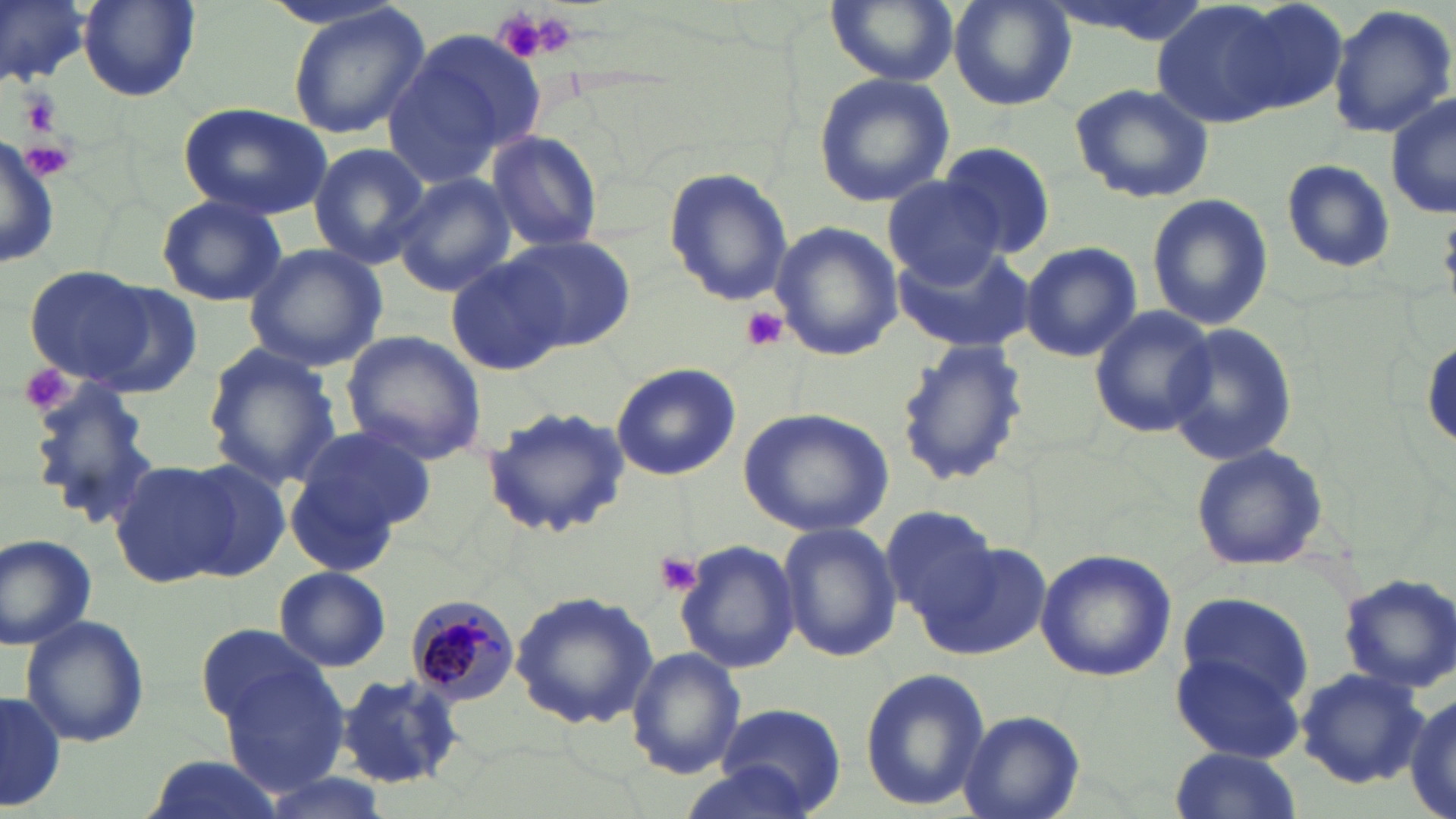

Approximate bounding boxes as (x1, y1, x2, y2) in pixels. Plasmodium malariae-infected red blood cell locations: (405, 594, 519, 707). Uninfected red blood cell locations: (0, 0, 89, 87), (824, 0, 959, 86), (948, 0, 1077, 111), (1149, 0, 1308, 130), (1210, 0, 1352, 120), (78, 1, 201, 102), (286, 3, 431, 141), (1327, 5, 1456, 140), (385, 27, 549, 185), (811, 72, 955, 209), (1068, 82, 1215, 205), (1387, 96, 1455, 221), (176, 101, 334, 220), (0, 131, 58, 276), (486, 133, 604, 255), (307, 142, 430, 269), (939, 143, 1056, 258), (1280, 159, 1396, 276), (662, 165, 793, 307), (390, 172, 517, 297), (881, 174, 1008, 287), (156, 193, 286, 308), (1145, 193, 1274, 330), (770, 223, 903, 361), (506, 235, 637, 349), (1019, 240, 1141, 363), (243, 242, 389, 371), (891, 245, 1031, 353), (444, 255, 568, 377), (23, 264, 156, 386), (80, 280, 206, 397), (1087, 305, 1216, 438), (1162, 320, 1299, 466), (341, 331, 486, 465), (1421, 334, 1455, 453), (893, 336, 1029, 490), (202, 343, 341, 489), (611, 363, 740, 481), (20, 378, 166, 531), (480, 405, 632, 543), (738, 407, 895, 537), (286, 431, 430, 571), (1189, 445, 1331, 572), (176, 461, 294, 583), (110, 462, 232, 588), (881, 505, 1000, 621), (776, 522, 901, 661), (0, 533, 96, 649), (918, 537, 1052, 661), (672, 538, 802, 674), (1034, 548, 1176, 684), (273, 565, 392, 671), (1337, 573, 1456, 693), (510, 591, 660, 729), (1169, 595, 1315, 756), (19, 612, 149, 749), (197, 624, 329, 728), (626, 646, 747, 778), (219, 662, 353, 795), (858, 667, 991, 811), (1295, 668, 1428, 789), (334, 671, 468, 789), (1, 689, 63, 814), (1405, 694, 1456, 819), (717, 699, 849, 814), (956, 710, 1084, 819), (1167, 748, 1305, 819), (137, 753, 285, 819), (676, 762, 824, 817), (254, 772, 393, 819). Platelet locations: (517, 8, 580, 61), (19, 90, 60, 135), (742, 306, 789, 353), (16, 363, 76, 416), (653, 552, 702, 597). Slide-level diagnosis: Plasmodium malariae. Thin blood smear. Light microscopy. Captured at 1000x magnification. Image is 1456×819 pixels. Single field of view. May-Grünwald-Giemsa stain.